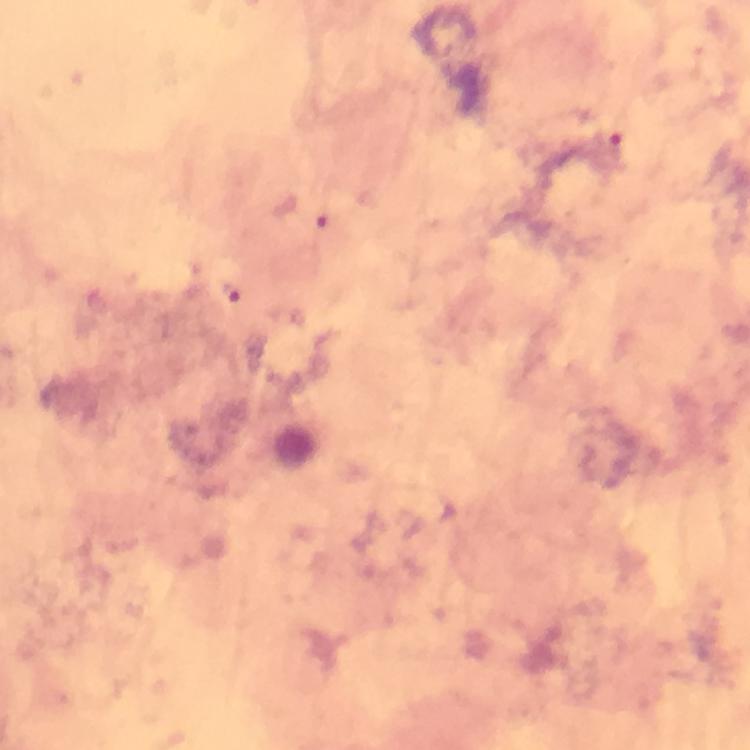

image size = 750×750 pixels
magnification = 100x
immersion oil = used
stain = Giemsa
cropped from = one field of view
capture = smartphone camera through the microscope
preparation = thick blood smear
context = from a malaria diagnostic workup
malaria parasite locations = approximate centers as {x, y} in pixels: {616, 143}, {231, 293}